Find each cell and give its type.
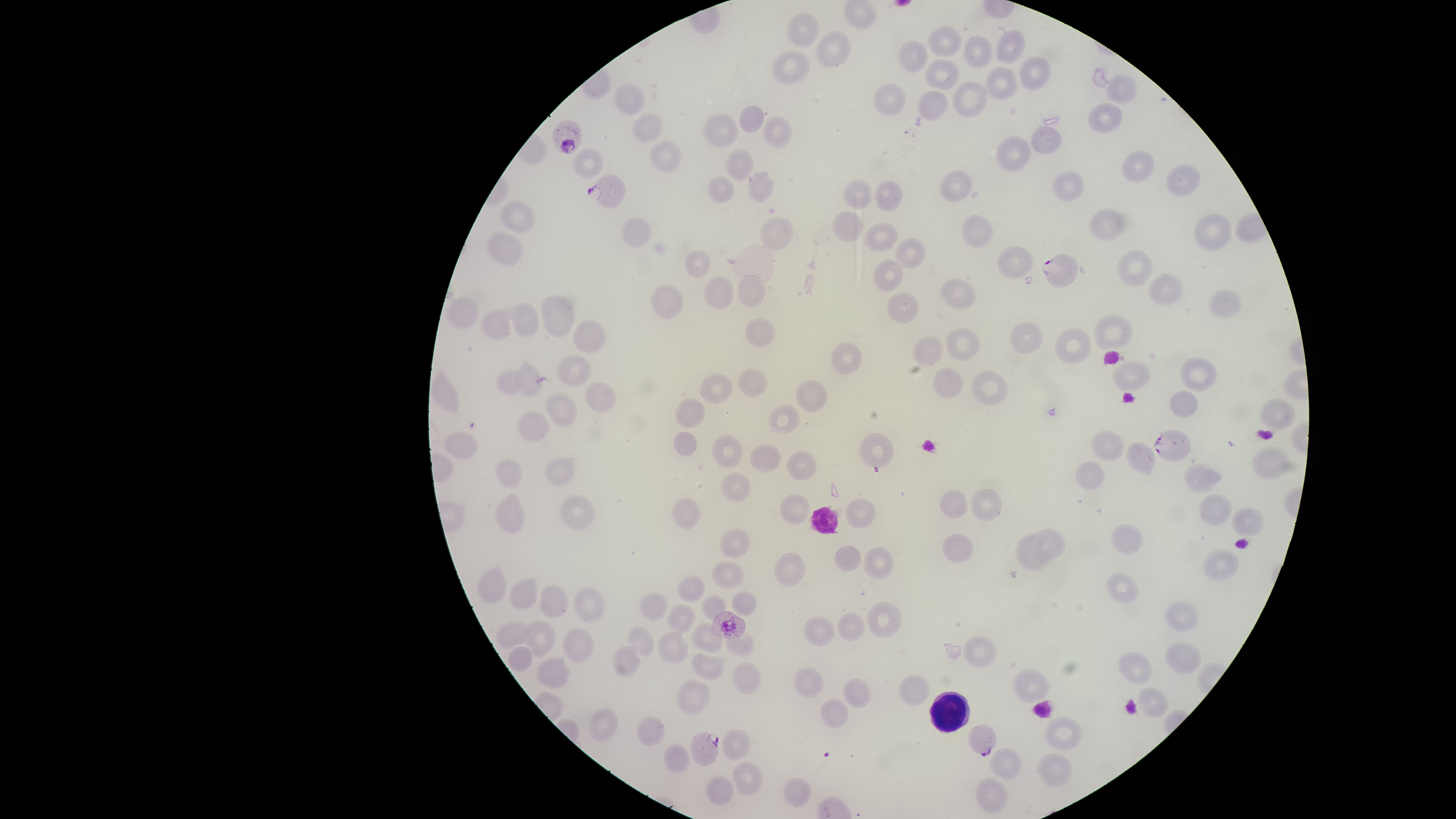

Approximate bounding boxes, in pixels from the top-left corner.
Parasitized RBCs: (left=551, top=120, right=583, bottom=154), (left=587, top=174, right=627, bottom=209), (left=1041, top=253, right=1079, bottom=289), (left=1153, top=429, right=1192, bottom=461), (left=711, top=610, right=746, bottom=639), (left=967, top=724, right=997, bottom=756), (left=689, top=731, right=719, bottom=766).
Uninfected RBCs: (left=842, top=0, right=878, bottom=31), (left=786, top=12, right=820, bottom=48), (left=927, top=25, right=962, bottom=57), (left=995, top=28, right=1026, bottom=63), (left=815, top=30, right=851, bottom=68), (left=962, top=35, right=993, bottom=68), (left=897, top=39, right=929, bottom=72), (left=771, top=50, right=811, bottom=85), (left=1018, top=55, right=1051, bottom=90), (left=924, top=58, right=960, bottom=90), (left=979, top=65, right=1019, bottom=101), (left=1104, top=73, right=1137, bottom=105), (left=951, top=80, right=988, bottom=117), (left=612, top=83, right=645, bottom=117), (left=873, top=83, right=906, bottom=116), (left=916, top=90, right=948, bottom=121), (left=1088, top=101, right=1122, bottom=133), (left=739, top=106, right=765, bottom=132), (left=631, top=112, right=663, bottom=144), (left=702, top=113, right=738, bottom=148), (left=761, top=116, right=792, bottom=149), (left=1030, top=125, right=1061, bottom=153), (left=996, top=136, right=1032, bottom=172), (left=649, top=139, right=682, bottom=173), (left=573, top=147, right=605, bottom=179), (left=724, top=149, right=754, bottom=182), (left=1121, top=150, right=1155, bottom=183), (left=1165, top=164, right=1201, bottom=197), (left=938, top=169, right=973, bottom=203), (left=746, top=170, right=775, bottom=204), (left=1053, top=171, right=1084, bottom=202), (left=707, top=175, right=735, bottom=203), (left=843, top=178, right=873, bottom=210), (left=873, top=179, right=903, bottom=212), (left=498, top=200, right=535, bottom=234), (left=1089, top=208, right=1126, bottom=242), (left=831, top=210, right=863, bottom=242), (left=1193, top=212, right=1232, bottom=251), (left=961, top=214, right=994, bottom=249), (left=758, top=216, right=793, bottom=250), (left=621, top=217, right=651, bottom=249), (left=864, top=222, right=899, bottom=252), (left=486, top=230, right=523, bottom=266), (left=894, top=237, right=928, bottom=269), (left=996, top=245, right=1033, bottom=280), (left=685, top=249, right=711, bottom=279), (left=1116, top=249, right=1152, bottom=287), (left=873, top=258, right=905, bottom=293), (left=736, top=273, right=766, bottom=309), (left=1147, top=273, right=1183, bottom=307), (left=703, top=274, right=735, bottom=309), (left=939, top=278, right=976, bottom=310), (left=651, top=283, right=685, bottom=320), (left=1208, top=289, right=1241, bottom=319), (left=886, top=291, right=920, bottom=324), (left=540, top=295, right=577, bottom=337), (left=446, top=296, right=479, bottom=329), (left=506, top=302, right=540, bottom=337), (left=479, top=306, right=512, bottom=341), (left=1093, top=313, right=1134, bottom=351), (left=745, top=317, right=775, bottom=348), (left=572, top=318, right=608, bottom=354), (left=1008, top=322, right=1043, bottom=356), (left=945, top=327, right=981, bottom=362), (left=1053, top=327, right=1093, bottom=364), (left=913, top=335, right=944, bottom=366), (left=830, top=342, right=862, bottom=374), (left=557, top=353, right=593, bottom=387), (left=1179, top=357, right=1217, bottom=391), (left=514, top=359, right=546, bottom=399), (left=1111, top=360, right=1151, bottom=391), (left=931, top=367, right=965, bottom=399), (left=737, top=368, right=768, bottom=398), (left=495, top=369, right=531, bottom=395), (left=970, top=371, right=1008, bottom=406), (left=698, top=373, right=733, bottom=404), (left=795, top=380, right=828, bottom=413), (left=584, top=381, right=618, bottom=414), (left=544, top=391, right=578, bottom=427), (left=1169, top=391, right=1198, bottom=418), (left=674, top=397, right=706, bottom=429), (left=1258, top=398, right=1296, bottom=430), (left=768, top=403, right=800, bottom=435), (left=516, top=409, right=550, bottom=443), (left=1090, top=430, right=1125, bottom=461), (left=441, top=431, right=478, bottom=460), (left=673, top=431, right=697, bottom=456), (left=859, top=432, right=893, bottom=467), (left=710, top=434, right=743, bottom=468), (left=1125, top=442, right=1156, bottom=477), (left=749, top=443, right=782, bottom=473), (left=1251, top=446, right=1289, bottom=480), (left=786, top=451, right=817, bottom=481), (left=544, top=456, right=576, bottom=487), (left=494, top=458, right=523, bottom=489), (left=1075, top=461, right=1104, bottom=490), (left=1183, top=462, right=1222, bottom=493), (left=719, top=471, right=750, bottom=503), (left=969, top=488, right=1002, bottom=521), (left=938, top=489, right=968, bottom=518), (left=493, top=493, right=526, bottom=535), (left=779, top=493, right=810, bottom=525), (left=1198, top=493, right=1232, bottom=527), (left=559, top=494, right=596, bottom=531), (left=671, top=497, right=701, bottom=529), (left=846, top=498, right=876, bottom=529), (left=1232, top=506, right=1263, bottom=536), (left=1111, top=523, right=1144, bottom=554), (left=718, top=527, right=750, bottom=559), (left=1028, top=527, right=1066, bottom=561), (left=1015, top=531, right=1049, bottom=571), (left=941, top=534, right=974, bottom=562), (left=835, top=546, right=862, bottom=572), (left=863, top=546, right=894, bottom=579), (left=1202, top=549, right=1239, bottom=582), (left=774, top=552, right=805, bottom=588), (left=711, top=561, right=743, bottom=589), (left=477, top=565, right=508, bottom=604), (left=1106, top=572, right=1139, bottom=604), (left=676, top=575, right=705, bottom=603), (left=508, top=576, right=538, bottom=611), (left=539, top=584, right=570, bottom=618), (left=573, top=585, right=606, bottom=623), (left=731, top=591, right=757, bottom=616), (left=638, top=592, right=668, bottom=621), (left=701, top=595, right=727, bottom=621), (left=1164, top=600, right=1200, bottom=633), (left=865, top=601, right=902, bottom=637), (left=666, top=604, right=696, bottom=633), (left=837, top=612, right=865, bottom=641), (left=803, top=616, right=835, bottom=646), (left=494, top=620, right=532, bottom=650), (left=521, top=620, right=556, bottom=658), (left=690, top=622, right=723, bottom=655), (left=627, top=625, right=656, bottom=656), (left=561, top=626, right=595, bottom=663), (left=657, top=630, right=688, bottom=664), (left=725, top=630, right=755, bottom=657), (left=963, top=635, right=998, bottom=669), (left=1165, top=640, right=1202, bottom=674), (left=613, top=644, right=641, bottom=678), (left=507, top=646, right=534, bottom=671), (left=690, top=651, right=726, bottom=680), (left=1118, top=651, right=1152, bottom=685), (left=535, top=656, right=572, bottom=689), (left=731, top=661, right=762, bottom=694), (left=793, top=667, right=823, bottom=698), (left=1011, top=668, right=1051, bottom=704), (left=898, top=675, right=931, bottom=706), (left=675, top=677, right=711, bottom=716), (left=842, top=678, right=871, bottom=708), (left=1136, top=686, right=1170, bottom=718), (left=820, top=697, right=849, bottom=728), (left=588, top=707, right=620, bottom=741), (left=635, top=716, right=664, bottom=745), (left=1044, top=716, right=1084, bottom=751), (left=720, top=728, right=751, bottom=760), (left=664, top=743, right=690, bottom=773), (left=988, top=747, right=1021, bottom=780), (left=1036, top=752, right=1073, bottom=787), (left=731, top=761, right=763, bottom=796), (left=706, top=776, right=734, bottom=806), (left=975, top=776, right=1008, bottom=814), (left=783, top=777, right=811, bottom=808).
WBCs: (left=929, top=692, right=970, bottom=733).

Giemsa-stained preparation. One field of view of the specimen. Image is 1456×819 pixels. Species: Plasmodium falciparum. The visible region is circular. Thin smear of blood. Photographed with a smartphone camera through the microscope eyepiece.